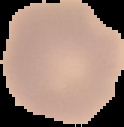
image type = segmented cell region with the area outside set to black
preparation = thin blood film
image size = 124×127 pixels
malaria status = uninfected